Locate Plasmodium falciparum parasites and identify their life-cycle stages.
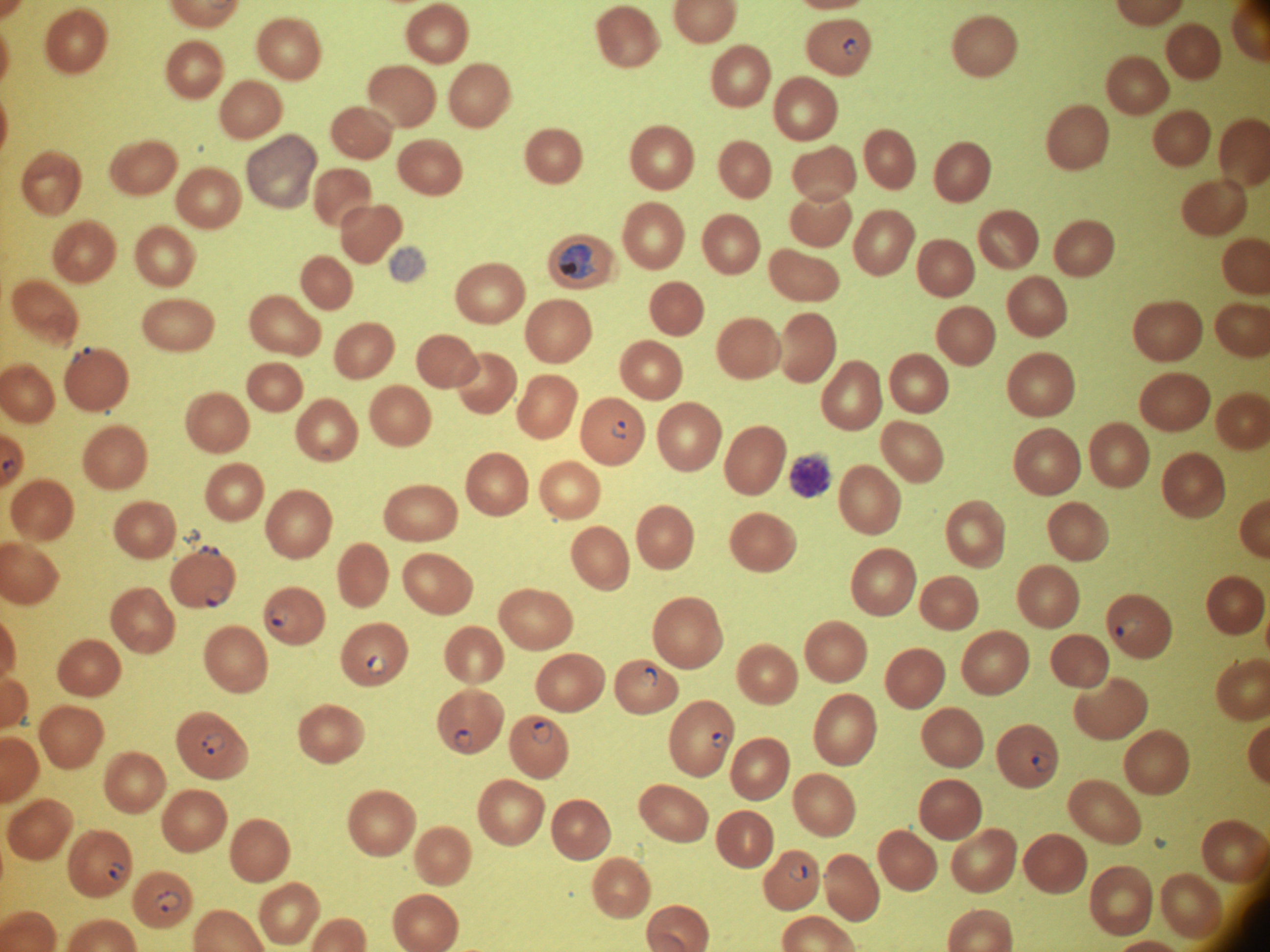
Approximate bounding boxes as (x1, y1, x2, y2) in pixels, from the source annotation, which is not necessarily exhaustive.
Ring forms: (612, 422, 632, 441), (207, 588, 226, 607), (269, 607, 293, 630), (1116, 616, 1139, 638), (368, 656, 385, 673), (641, 669, 659, 687), (533, 723, 550, 740), (456, 730, 472, 746), (202, 733, 225, 756), (711, 733, 727, 748), (1032, 753, 1054, 774), (789, 863, 807, 881), (107, 864, 124, 881), (158, 891, 180, 913).
Trophozoites: (560, 244, 593, 279).

life_cycle_stages_among_the_annotated_parasites: ring form, trophozoite
image_size: 1270×952 pixels
magnification: 100x
field_of_view: one from this slide
species: Plasmodium falciparum
microscope: Leica DM2000 with built-in camera
preparation: thin blood smear
stain: Giemsa